State which parasite is depicted.
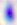

Toxoplasma gondii.

Photomicrograph. 400x magnification.